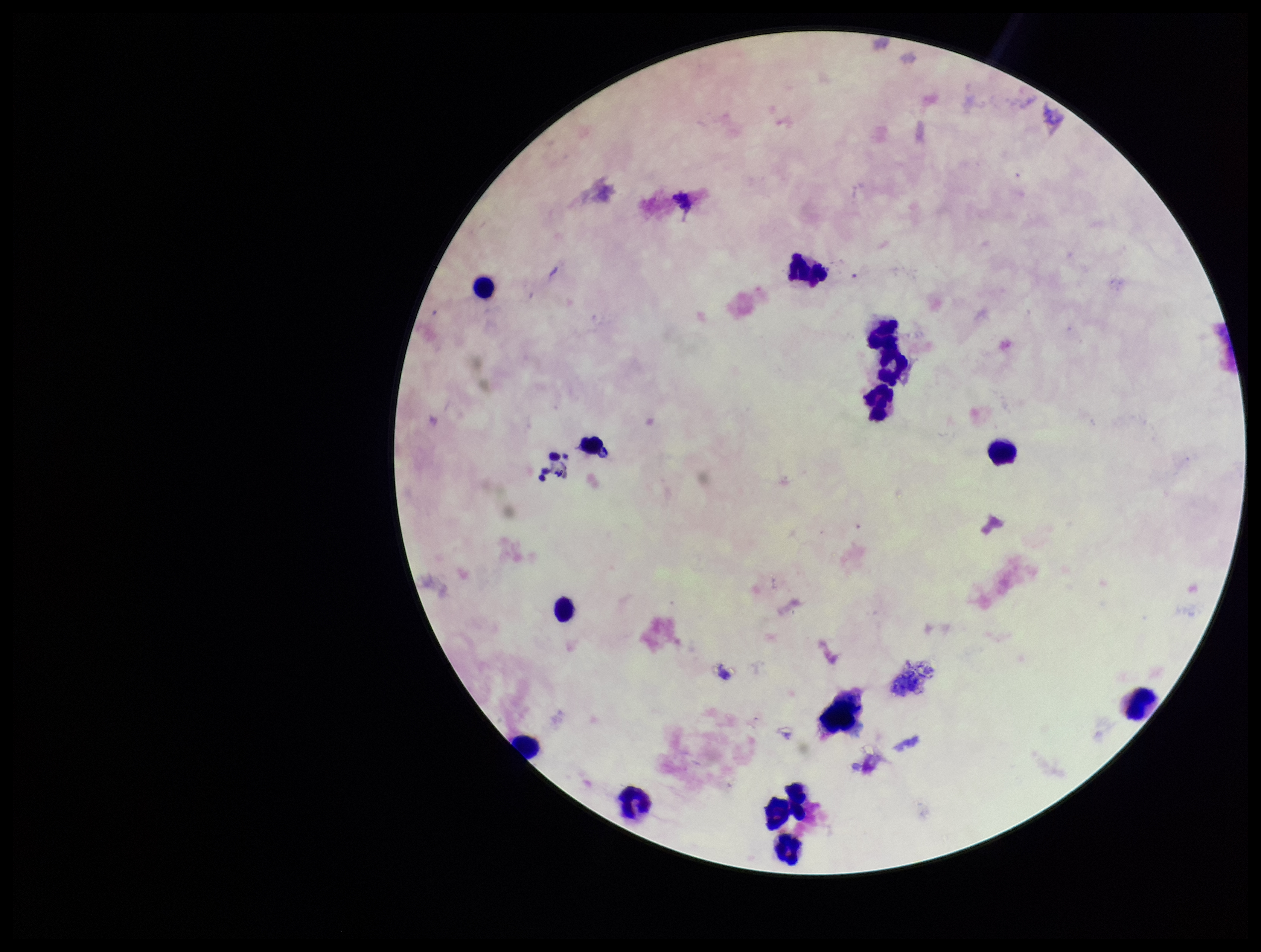

Summary:
  - Preparation: thick
  - Field of view: single
  - Leukocyte count: 14
  - Patient malaria status: infected
  - Capture: smartphone photograph through the microscope eyepiece
  - Parasite count: 0
  - Species reported for this patient: Plasmodium falciparum
  - Plasmodium parasites: none seen
  - Image size: 1261×952 pixels
  - Stain: Giemsa